Point out each malaria parasite.
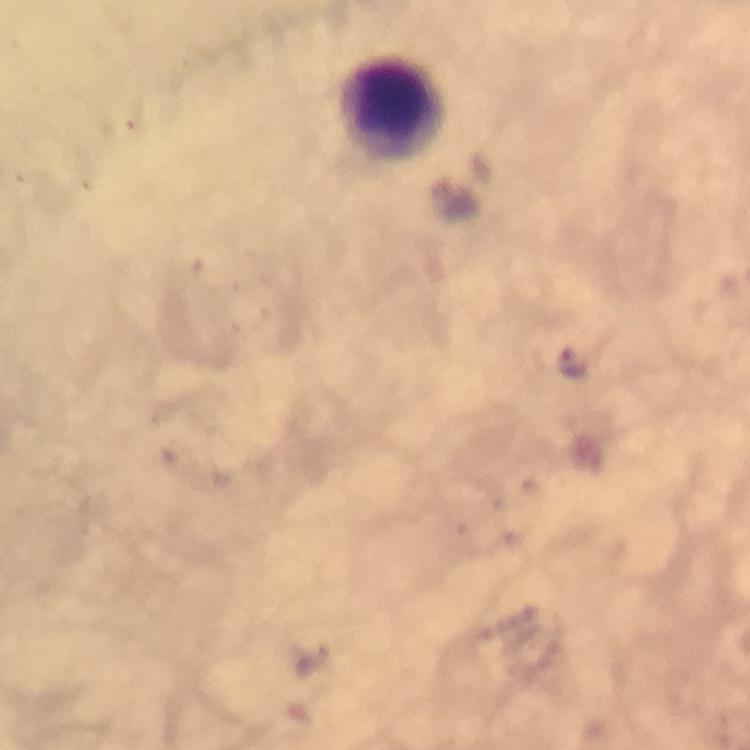
Approximate centers as (x, y) in pixels.
Malaria parasites: (572, 362).

Summary:
  - Leukocyte locations: (391, 110)
  - Preparation: thick blood smear
  - Stain: Giemsa
  - Magnification: 100x
  - Immersion oil: applied
  - Context: from a diagnostic examination for malaria
  - Cropped from: a single field of view
  - Capture: smartphone mounted on the microscope
  - Image size: 750×750 pixels